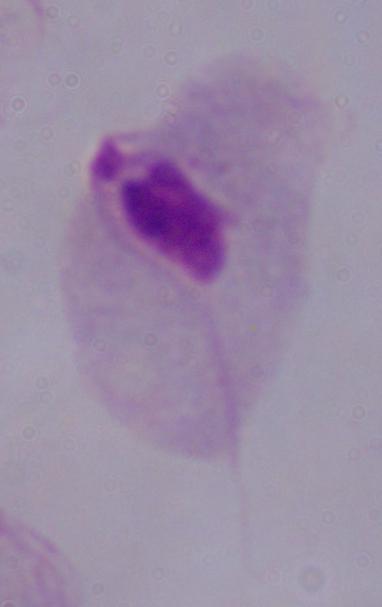
Micrograph. 1000x magnification. A trichomonad is seen.